Assess this cell for malaria.
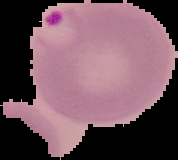

It is parasitized.

Image is 178×160 pixels. The area outside the segmented cell region is set to black. From a thin blood smear.